Identify the blood parasite species.
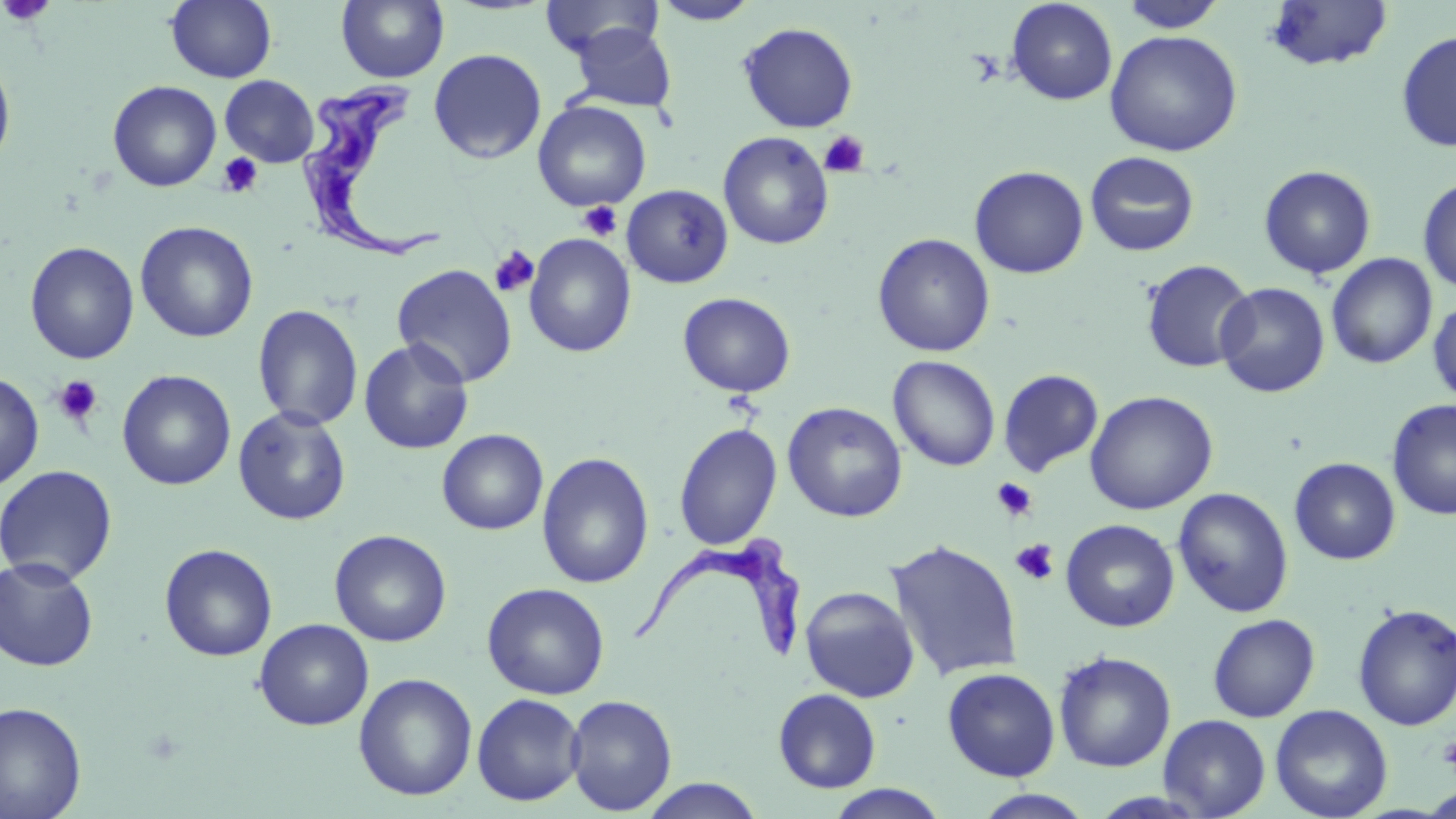
Trypanosoma brucei.

platelet locations = approximate bounding boxes as named x1/y1/x2/y2 corners in pixels: (x1=1, y1=0, x2=56, y2=27), (x1=819, y1=130, x2=870, y2=178), (x1=217, y1=152, x2=264, y2=198), (x1=576, y1=200, x2=623, y2=240), (x1=489, y1=246, x2=539, y2=297), (x1=53, y1=375, x2=103, y2=426), (x1=991, y1=478, x2=1037, y2=522), (x1=1010, y1=539, x2=1059, y2=585), (x1=1439, y1=735, x2=1456, y2=775)
modality = optical microscopy
stain = May-Grünwald-Giemsa
Trypanosoma brucei locations = approximate bounding boxes as named x1/y1/x2/y2 corners in pixels: (x1=299, y1=78, x2=445, y2=264), (x1=626, y1=534, x2=808, y2=664)
field of view = single
uninfected red blood cell locations = approximate bounding boxes as named x1/y1/x2/y2 corners in pixels: (x1=336, y1=0, x2=449, y2=84), (x1=540, y1=0, x2=663, y2=59), (x1=1263, y1=0, x2=1395, y2=73), (x1=166, y1=1, x2=277, y2=83), (x1=651, y1=1, x2=761, y2=26), (x1=1005, y1=1, x2=1118, y2=106), (x1=1118, y1=1, x2=1227, y2=33), (x1=737, y1=21, x2=859, y2=133), (x1=569, y1=23, x2=677, y2=112), (x1=1105, y1=29, x2=1242, y2=156), (x1=1396, y1=31, x2=1456, y2=153), (x1=428, y1=48, x2=546, y2=165), (x1=0, y1=53, x2=16, y2=173), (x1=220, y1=75, x2=319, y2=167), (x1=107, y1=80, x2=222, y2=192), (x1=533, y1=100, x2=651, y2=211), (x1=719, y1=132, x2=833, y2=250), (x1=1085, y1=151, x2=1200, y2=257), (x1=1258, y1=165, x2=1377, y2=279), (x1=969, y1=166, x2=1089, y2=278), (x1=1417, y1=176, x2=1456, y2=294), (x1=621, y1=185, x2=733, y2=288), (x1=135, y1=221, x2=258, y2=343), (x1=523, y1=233, x2=636, y2=357), (x1=872, y1=233, x2=995, y2=357), (x1=24, y1=241, x2=140, y2=364), (x1=1326, y1=253, x2=1438, y2=370), (x1=1140, y1=259, x2=1255, y2=374), (x1=392, y1=264, x2=517, y2=388), (x1=1215, y1=282, x2=1330, y2=398), (x1=677, y1=292, x2=796, y2=397), (x1=1428, y1=297, x2=1456, y2=407), (x1=252, y1=303, x2=363, y2=430), (x1=358, y1=337, x2=474, y2=455), (x1=888, y1=355, x2=1000, y2=471), (x1=998, y1=368, x2=1104, y2=477), (x1=116, y1=369, x2=236, y2=490), (x1=0, y1=370, x2=44, y2=492), (x1=1084, y1=390, x2=1218, y2=515), (x1=1386, y1=398, x2=1456, y2=521), (x1=782, y1=401, x2=907, y2=523), (x1=233, y1=406, x2=351, y2=525), (x1=674, y1=423, x2=782, y2=550), (x1=436, y1=429, x2=549, y2=535), (x1=537, y1=452, x2=654, y2=589), (x1=1289, y1=457, x2=1400, y2=565), (x1=0, y1=464, x2=118, y2=585), (x1=1173, y1=487, x2=1294, y2=618), (x1=1061, y1=519, x2=1180, y2=632), (x1=329, y1=529, x2=451, y2=647), (x1=885, y1=538, x2=1023, y2=681), (x1=159, y1=543, x2=278, y2=662), (x1=1, y1=556, x2=100, y2=671), (x1=482, y1=582, x2=610, y2=700), (x1=799, y1=585, x2=920, y2=703), (x1=1352, y1=604, x2=1456, y2=731), (x1=1208, y1=613, x2=1320, y2=722), (x1=254, y1=618, x2=374, y2=730), (x1=1053, y1=650, x2=1177, y2=772), (x1=942, y1=667, x2=1060, y2=782), (x1=353, y1=673, x2=477, y2=801), (x1=773, y1=688, x2=881, y2=793), (x1=471, y1=693, x2=585, y2=806), (x1=565, y1=694, x2=677, y2=815), (x1=0, y1=701, x2=87, y2=819), (x1=1269, y1=704, x2=1393, y2=819), (x1=1158, y1=714, x2=1271, y2=818), (x1=636, y1=778, x2=766, y2=818), (x1=823, y1=784, x2=952, y2=819), (x1=971, y1=789, x2=1097, y2=819)
image size = 1456×819 pixels
preparation = thin blood smear
magnification = 1000x